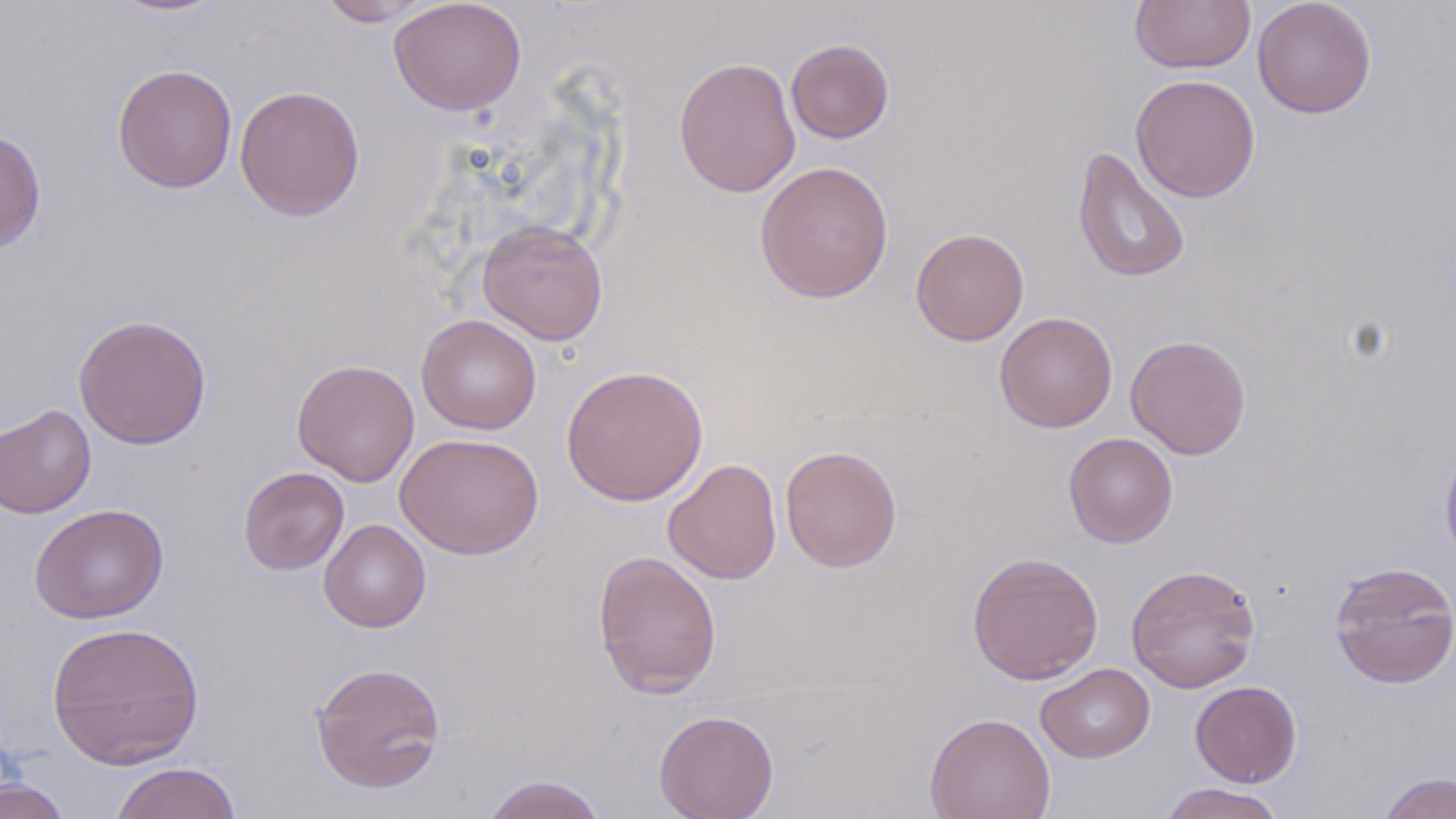 Approximate bounding boxes as (x1,y1)-(x2,y2) corner pairs in pixels. Uninfected red blood cell locations: (104,0)-(232,17), (314,0)-(442,27), (389,0)-(527,116), (1130,0)-(1255,74), (1252,0)-(1377,118), (786,39)-(895,143), (673,56)-(801,198), (112,63)-(238,194), (1131,74)-(1261,203), (234,84)-(365,221), (0,129)-(47,255), (1072,145)-(1191,285), (754,160)-(894,304), (477,219)-(609,346), (911,227)-(1029,346), (994,312)-(1118,433), (73,314)-(212,450), (416,314)-(542,434), (1125,334)-(1252,460), (292,359)-(420,487), (561,364)-(709,506), (0,404)-(96,519), (395,432)-(544,559), (1063,432)-(1178,548), (1439,439)-(1456,570), (779,445)-(903,572), (662,458)-(782,585), (238,467)-(350,575), (29,503)-(168,624), (318,518)-(431,633), (592,548)-(723,699), (967,550)-(1104,685), (1329,561)-(1456,688), (1125,563)-(1260,692), (46,621)-(205,769), (310,660)-(447,794), (1036,663)-(1155,763), (1190,680)-(1302,787), (653,709)-(779,819), (924,711)-(1055,819), (108,762)-(242,819), (1379,771)-(1455,819), (479,773)-(609,819), (0,777)-(73,819), (1156,783)-(1287,819). Slide-level diagnosis: no evidence of blood parasites. May-Grünwald-Giemsa stain. Single field of view. Optical microscopy. Image is 1456×819 pixels. Thin blood smear. 1000x magnification.